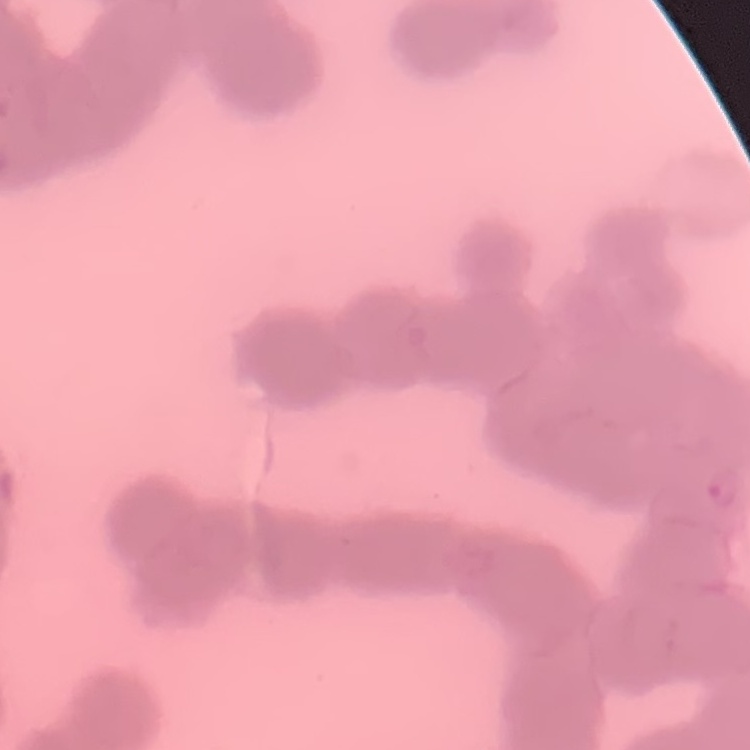

Summary:
  - Erythrocyte morphology: rouleaux formation
  - Preparation: thin peripheral smear
  - Stain: Field's or Giemsa
  - Image type: one tile cut from a larger photomicrograph